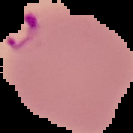
malaria status = parasitized
image size = 133×133 pixels
preparation = thin blood smear
image type = cell region segmented out of the field of view; surrounding area masked to black